Describe the morphology of the erythrocytes.
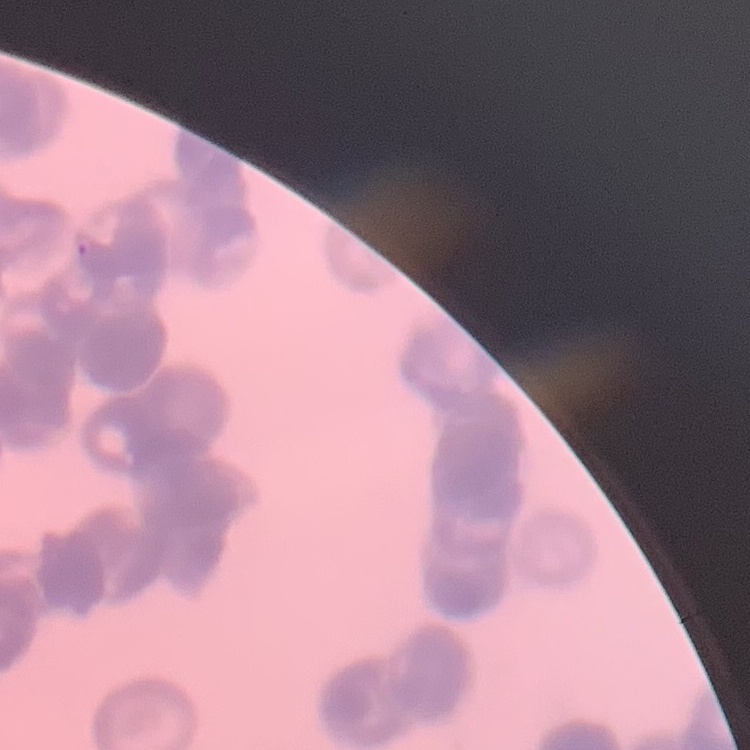

Rouleaux formation.

Summary:
  - Preparation: thin peripheral smear
  - Stain: Field's or Giemsa
  - Image type: one tile cut from a larger photomicrograph